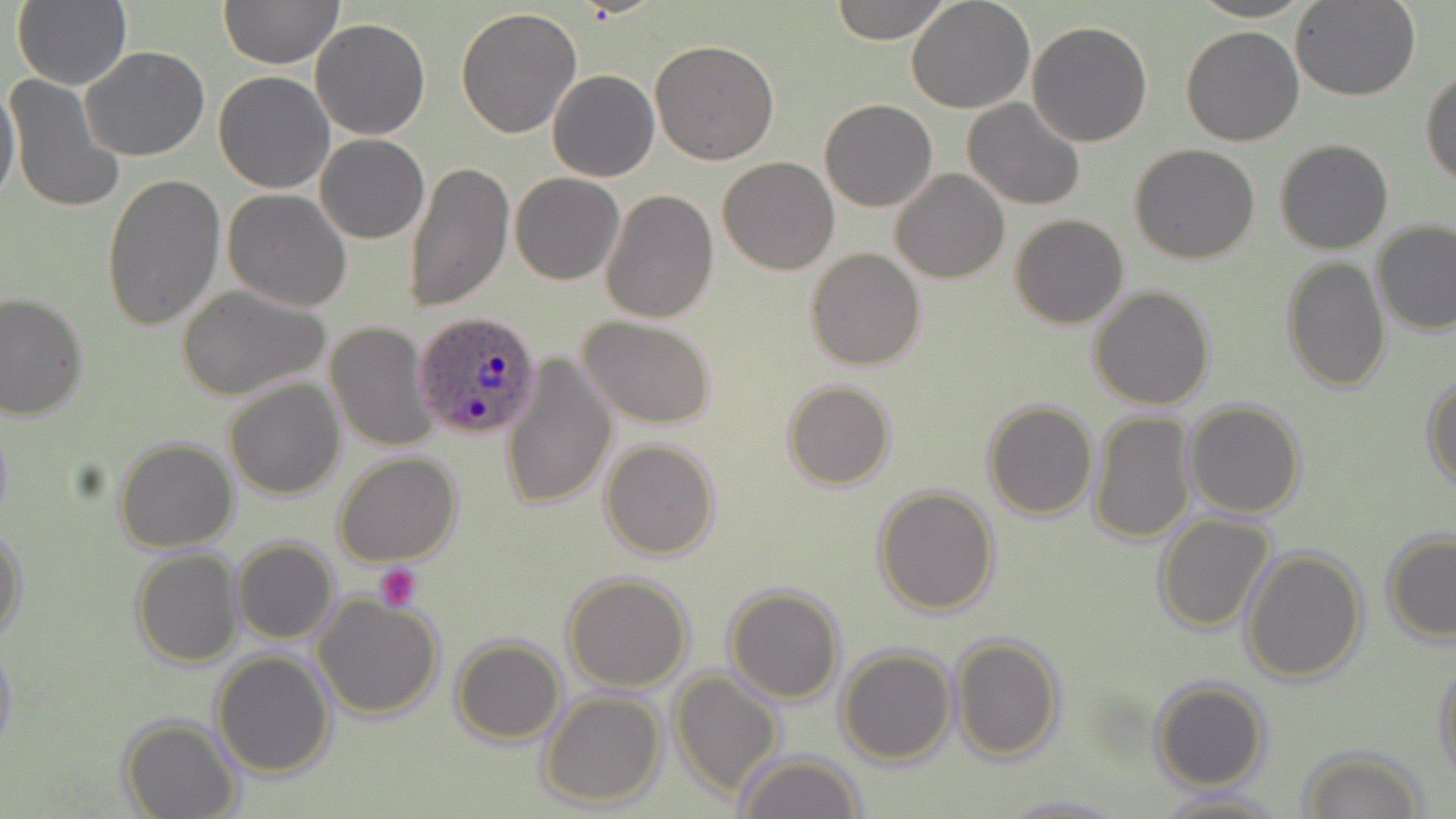

Plasmodium ovale-infected red blood cell locations = approximate bounding boxes as (x1, y1, x2, y2) in pixels: (415, 311, 543, 439)
slide-level diagnosis = Plasmodium ovale
platelet locations = approximate bounding boxes as (x1, y1, x2, y2) in pixels: (372, 562, 423, 611)
field of view = single
uninfected red blood cell locations = approximate bounding boxes as (x1, y1, x2, y2) in pixels: (12, 0, 131, 91), (219, 0, 343, 69), (829, 0, 952, 44), (906, 0, 1036, 114), (1189, 0, 1314, 22), (1292, 0, 1420, 101), (457, 8, 583, 140), (310, 18, 431, 139), (1025, 21, 1153, 148), (1180, 26, 1305, 147), (650, 41, 779, 164), (80, 46, 211, 161), (1421, 68, 1455, 187), (547, 69, 659, 182), (213, 71, 337, 194), (5, 74, 125, 216), (0, 75, 21, 210), (963, 99, 1085, 210), (820, 100, 937, 213), (315, 134, 429, 243), (1274, 138, 1393, 255), (1129, 144, 1260, 263), (718, 156, 838, 275), (405, 159, 514, 312), (890, 168, 1009, 284), (509, 173, 624, 284), (100, 174, 225, 332), (601, 188, 719, 322), (222, 189, 352, 312), (1009, 214, 1128, 328), (1372, 220, 1456, 335), (805, 248, 925, 370), (1280, 256, 1390, 393), (176, 284, 334, 403), (1088, 286, 1216, 410), (0, 292, 88, 424), (576, 315, 716, 427), (324, 321, 438, 452), (500, 354, 615, 511), (1422, 371, 1455, 491), (224, 377, 346, 500), (783, 381, 895, 491), (981, 400, 1100, 520), (1183, 400, 1306, 517), (1088, 411, 1196, 544), (0, 416, 13, 533), (114, 437, 238, 552), (600, 438, 721, 559), (332, 453, 461, 569), (873, 485, 999, 616), (1154, 512, 1276, 633), (0, 524, 26, 641), (1381, 530, 1456, 644), (232, 538, 338, 644), (131, 548, 244, 666), (1241, 549, 1368, 683), (563, 572, 694, 692), (722, 583, 847, 704), (312, 590, 444, 719), (0, 635, 17, 763), (949, 635, 1064, 761), (450, 637, 565, 745), (837, 645, 957, 766), (211, 651, 338, 779), (1432, 655, 1456, 781), (668, 669, 784, 799), (1149, 680, 1272, 791), (539, 689, 667, 808), (118, 715, 242, 819), (1299, 747, 1430, 819), (734, 751, 866, 819), (1152, 789, 1286, 819), (995, 794, 1131, 818)
magnification = 1000x
modality = optical microscopy
stain = May-Grünwald-Giemsa
preparation = thin blood smear
image size = 1456×819 pixels